State which parasite is depicted.
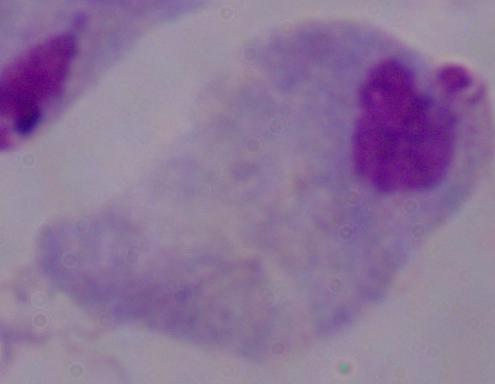

A trichomonad.

1000x magnification. Micrograph.